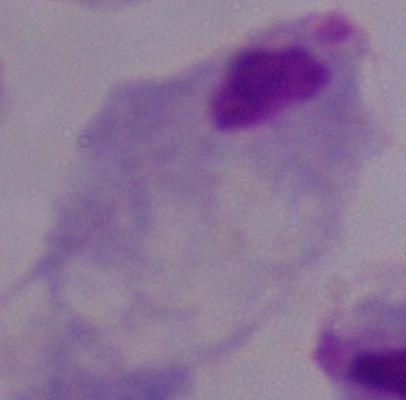
identification: trichomonad
modality: photomicrograph
magnification: 1000x